Assess this cell for malaria.
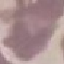
Uninfected.

Summary:
  - Preparation: thin smear
  - Capture: smartphone camera at the microscope eyepiece
  - Image type: cell patch, automatically extracted from a larger field of view and resized to 64 × 64 pixels
  - Stain: Giemsa